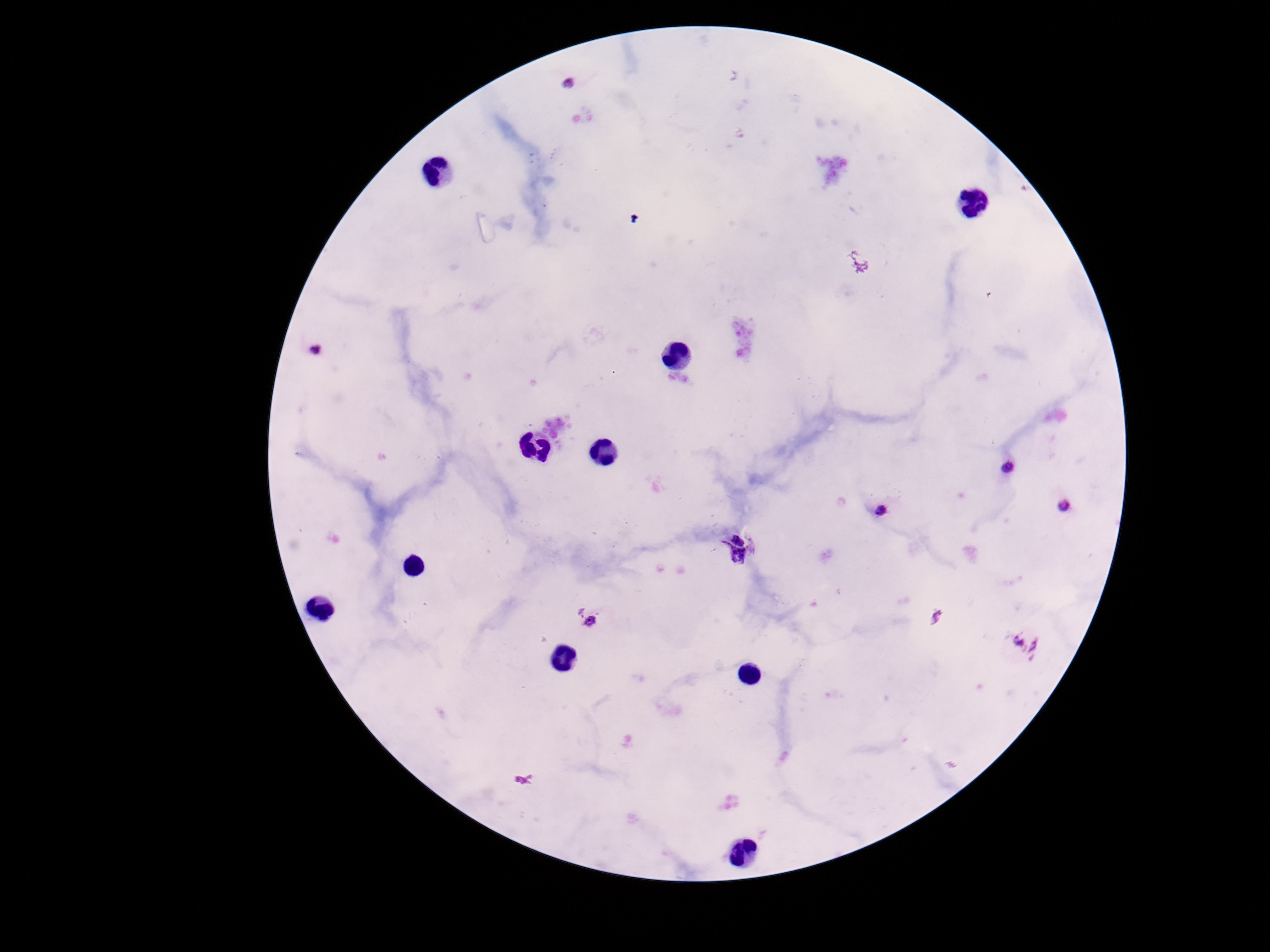
preparation = thick blood smear
capture = smartphone camera through the microscope eyepiece
stain = Giemsa
magnification = 100x
patient malaria status = positive
field of view = one from this slide
Plasmodium parasite locations = approximate centers as {x, y} in pixels: {567, 84}, {316, 348}, {1009, 468}, {1065, 504}, {882, 509}, {736, 548}, {586, 619}, {1028, 643}
image size = 1270×952 pixels